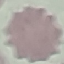
Malaria status: uninfected. Acquired by smartphone through the microscope eyepiece. Cell patch, automatically extracted from a larger field of view and resized to 64 × 64 pixels. Giemsa-stained preparation. Thin blood smear.